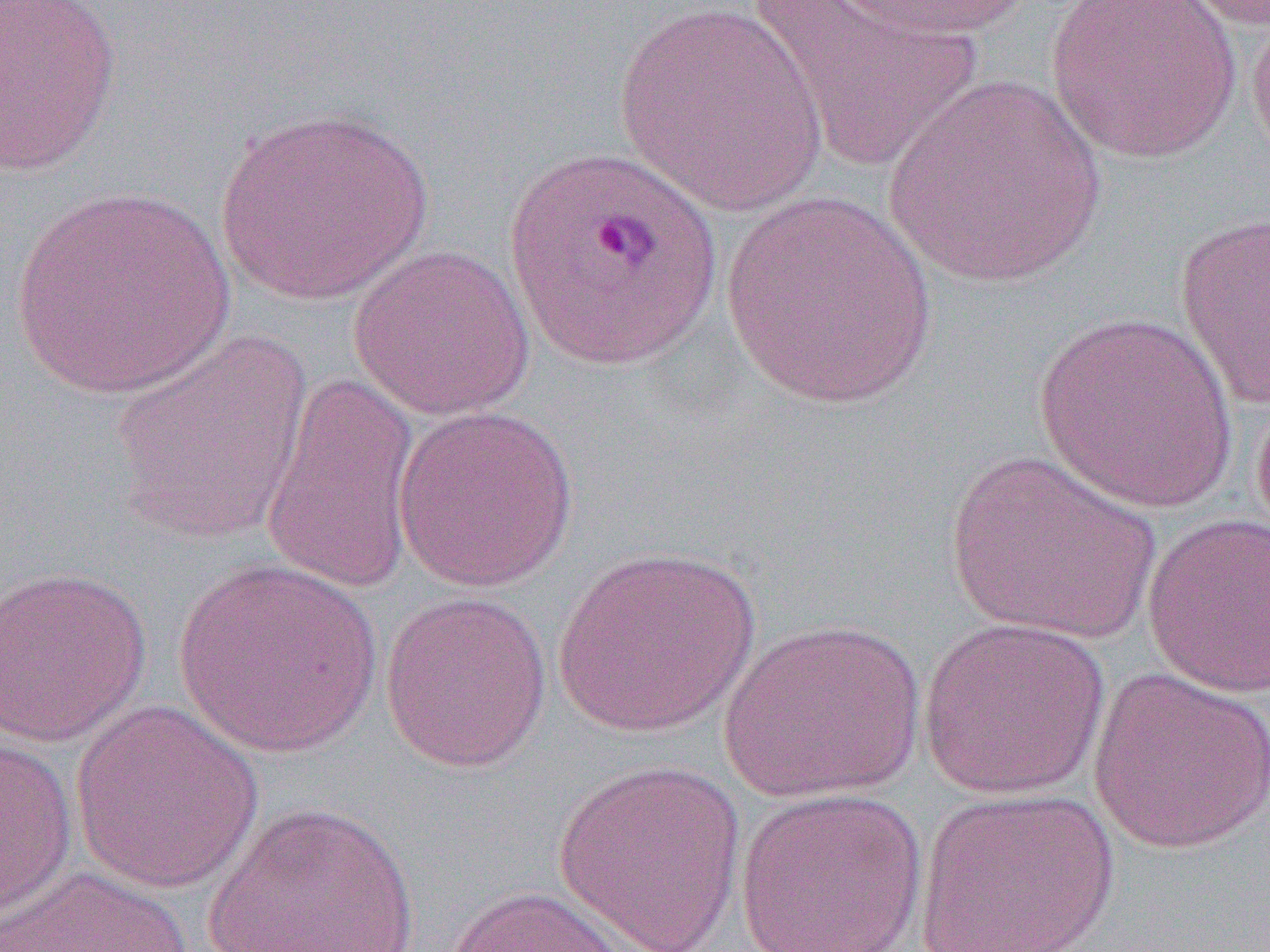
Approximate bounding boxes as (x1,y1)-(x2,y2) corner pairs in pixels. Plasmodium ovale-infected red blood cell locations: (503,144)-(724,375). Uninfected red blood cell locations: (0,0)-(123,176), (746,0)-(982,173), (823,0)-(1037,41), (1044,0)-(1243,164), (1177,0)-(1270,33), (612,3)-(831,217), (1246,7)-(1270,176), (883,74)-(1108,290), (216,106)-(434,306), (9,185)-(235,399), (719,190)-(941,410), (1174,212)-(1270,411), (347,244)-(536,421), (1033,311)-(1240,514), (110,332)-(315,546), (260,373)-(422,596), (1251,380)-(1270,555), (393,406)-(579,593), (943,449)-(1163,644), (1141,512)-(1270,698), (551,544)-(762,738), (172,559)-(384,758), (0,564)-(152,748), (379,589)-(553,772), (917,616)-(1111,800), (718,618)-(925,803), (1088,666)-(1270,855), (70,700)-(265,895), (0,738)-(77,922), (553,757)-(748,951), (914,786)-(1120,952), (735,787)-(927,951), (202,801)-(420,952), (1,864)-(193,952), (445,885)-(654,952). Slide-level diagnosis: Plasmodium ovale. Image is 1270×952 pixels. 1000x magnification. Optical microscopy. One field of a larger specimen. Thin blood film.